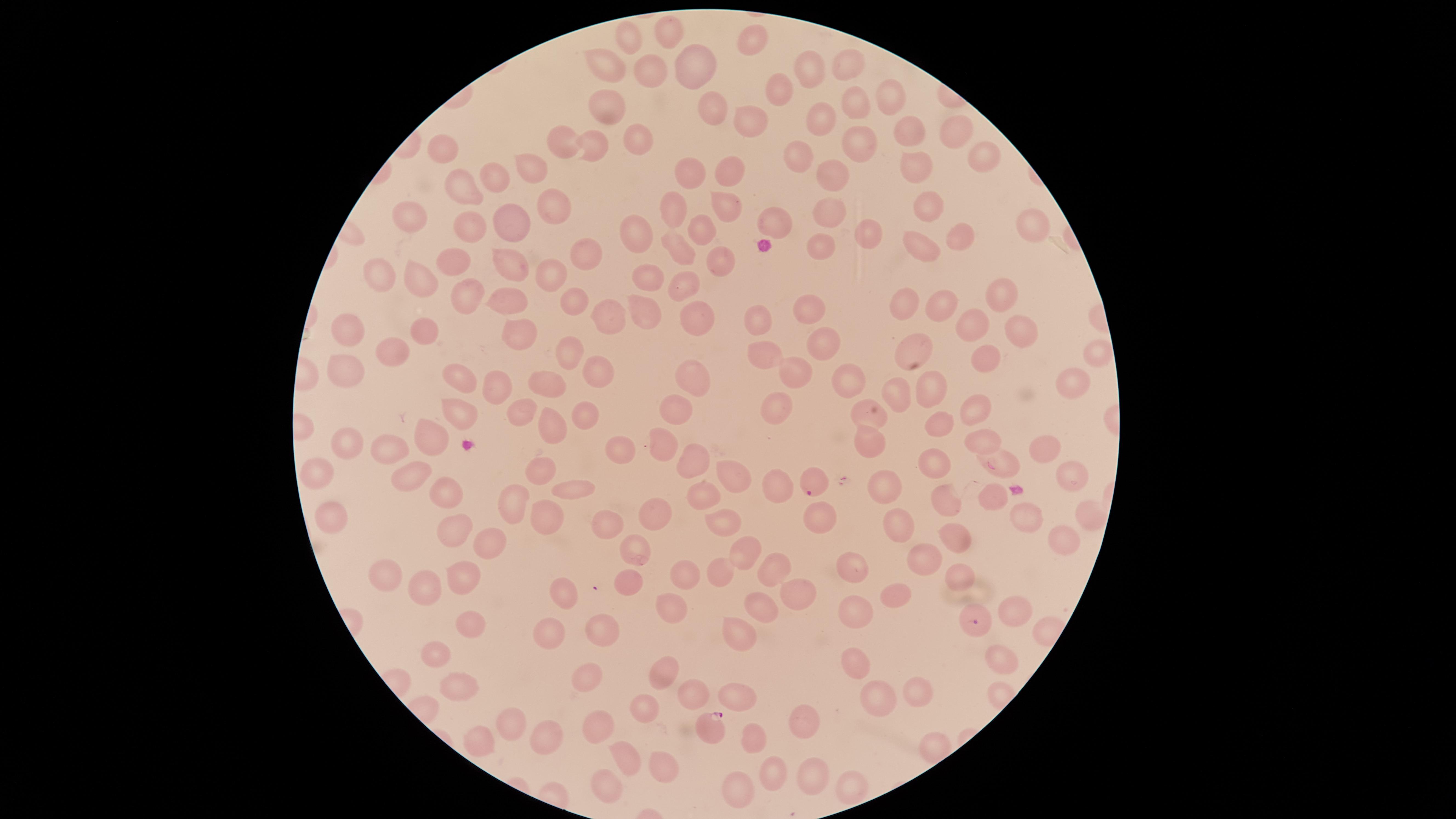
{
  "stain": "Giemsa",
  "species": "Plasmodium falciparum",
  "parasitized_RBCs": "approximate marker points as {x, y} in pixels: {998, 464}, {813, 481}, {978, 623}, {712, 728}",
  "uninfected_RBCs": "approximate marker points as {x, y} in pixels: {669, 32}, {755, 34}, {630, 35}, {608, 65}, {845, 65}, {696, 68}, {810, 71}, {646, 72}, {779, 88}, {887, 92}, {853, 105}, {605, 106}, {716, 113}, {820, 115}, {747, 123}, {955, 124}, {914, 128}, {568, 136}, {635, 137}, {859, 145}, {443, 147}, {592, 148}, {985, 156}, {802, 159}, {532, 167}, {914, 167}, {727, 169}, {692, 170}, {833, 175}, {493, 177}, {462, 188}, {553, 203}, {929, 203}, {727, 205}, {677, 208}, {828, 211}, {410, 219}, {512, 220}, {778, 221}, {466, 225}, {1035, 225}, {638, 229}, {698, 232}, {867, 235}, {960, 236}, {679, 245}, {820, 245}, {918, 245}, {589, 259}, {724, 260}, {460, 261}, {509, 266}, {550, 270}, {382, 274}, {421, 278}, {650, 281}, {683, 285}, {999, 291}, {472, 295}, {511, 300}, {577, 300}, {942, 301}, {910, 302}, {806, 305}, {642, 307}, {611, 313}, {696, 316}, {756, 323}, {975, 325}, {420, 328}, {341, 329}, {1021, 329}, {519, 333}, {820, 340}, {914, 345}, {393, 346}, {568, 350}, {763, 355}, {1097, 355}, {987, 356}, {346, 365}, {687, 367}, {796, 369}, {596, 370}, {453, 376}, {853, 376}, {493, 379}, {1069, 382}, {551, 384}, {931, 387}, {896, 392}, {680, 401}, {778, 401}, {977, 405}, {521, 409}, {456, 413}, {581, 413}, {865, 413}, {941, 423}, {549, 424}, {983, 436}, {429, 439}, {865, 440}, {662, 442}, {349, 444}, {386, 446}, {620, 451}, {1042, 451}, {688, 460}, {932, 463}, {539, 469}, {411, 472}, {321, 474}, {731, 477}, {1066, 484}, {774, 485}, {439, 487}, {564, 489}, {880, 489}, {705, 490}, {950, 497}, {516, 505}, {330, 512}, {655, 512}, {820, 514}, {1090, 515}, {1029, 517}, {543, 518}, {722, 522}, {900, 524}, {610, 527}, {451, 528}, {489, 537}, {958, 538}, {1059, 539}, {739, 548}, {634, 551}, {922, 558}, {851, 566}, {772, 568}, {383, 571}, {679, 573}, {723, 573}, {463, 575}, {957, 576}, {627, 581}, {426, 584}, {558, 595}, {891, 595}, {792, 596}, {762, 606}, {666, 608}, {857, 610}, {1013, 613}, {470, 620}, {735, 629}, {550, 630}, {604, 630}, {435, 652}, {854, 655}, {1002, 659}, {665, 671}, {583, 672}, {461, 681}, {689, 692}, {917, 692}, {738, 693}, {879, 693}, {644, 709}, {804, 717}, {507, 718}, {599, 726}, {537, 735}, {757, 736}, {478, 740}, {624, 757}, {662, 766}, {774, 772}, {812, 777}, {605, 782}, {738, 782}, {849, 788}",
  "image_size": "1456×819 pixels",
  "preparation": "thin blood film",
  "capture": "smartphone photograph through the microscope eyepiece",
  "visible_region": "circular",
  "presence": "malaria parasites detected",
  "field_of_view": "single"
}